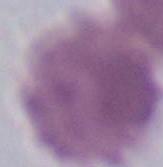

{
  "modality": "photomicrograph",
  "magnification": "1000x",
  "identification": "erythrocyte"
}